Name the parasite shown.
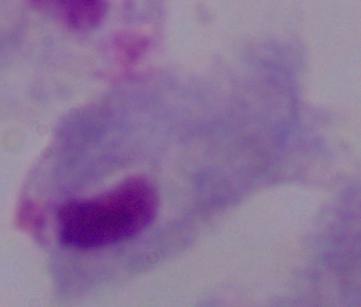
A trichomonad.

{
  "modality": "photomicrograph",
  "magnification": "1000x"
}